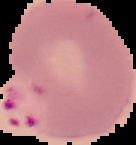

Segmented cell region on a black background. Image is 136×145 pixels. Result: malaria parasites detected. From a thin blood smear.